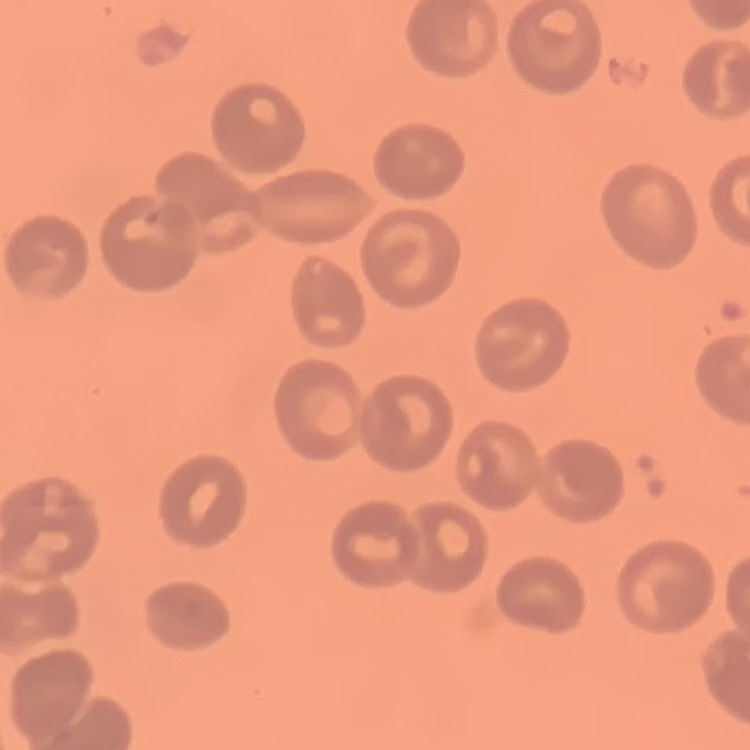

The erythrocytes show no rouleaux formation. Thin blood smear. Stained with either Field's or Giemsa. Square crop of a larger photomicrograph.